Comment on the morphology of the erythrocytes.
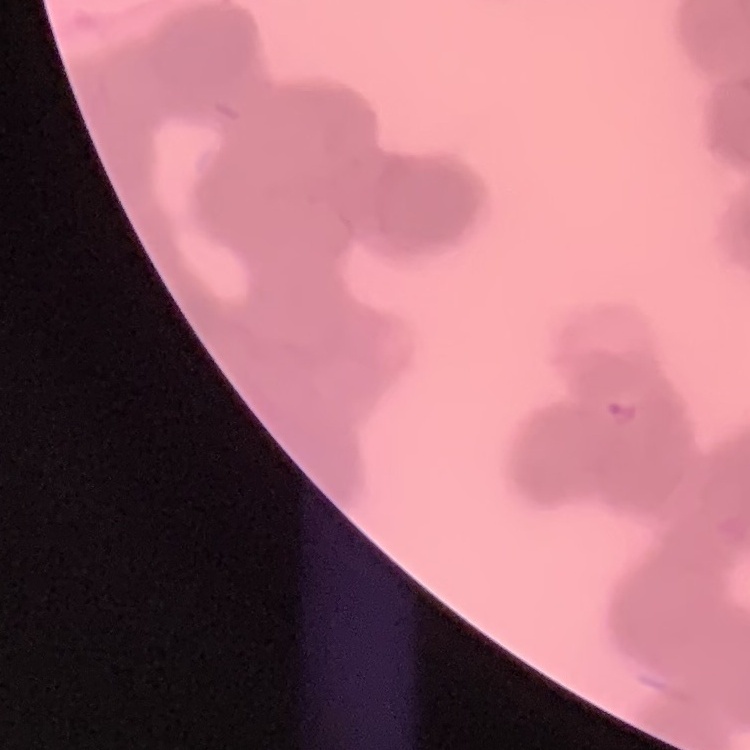

Rouleaux formation.

preparation: thin blood film
image_type: square crop of a larger photomicrograph
stain: Field's or Giemsa